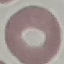
Summary:
  - Result: no malaria parasites detected
  - Image type: cell patch, automatically extracted from a larger field of view and resized to 64 × 64 pixels
  - Stain: Giemsa
  - Capture: smartphone camera at the microscope eyepiece
  - Preparation: thin smear